Locate and identify every blood parasite.
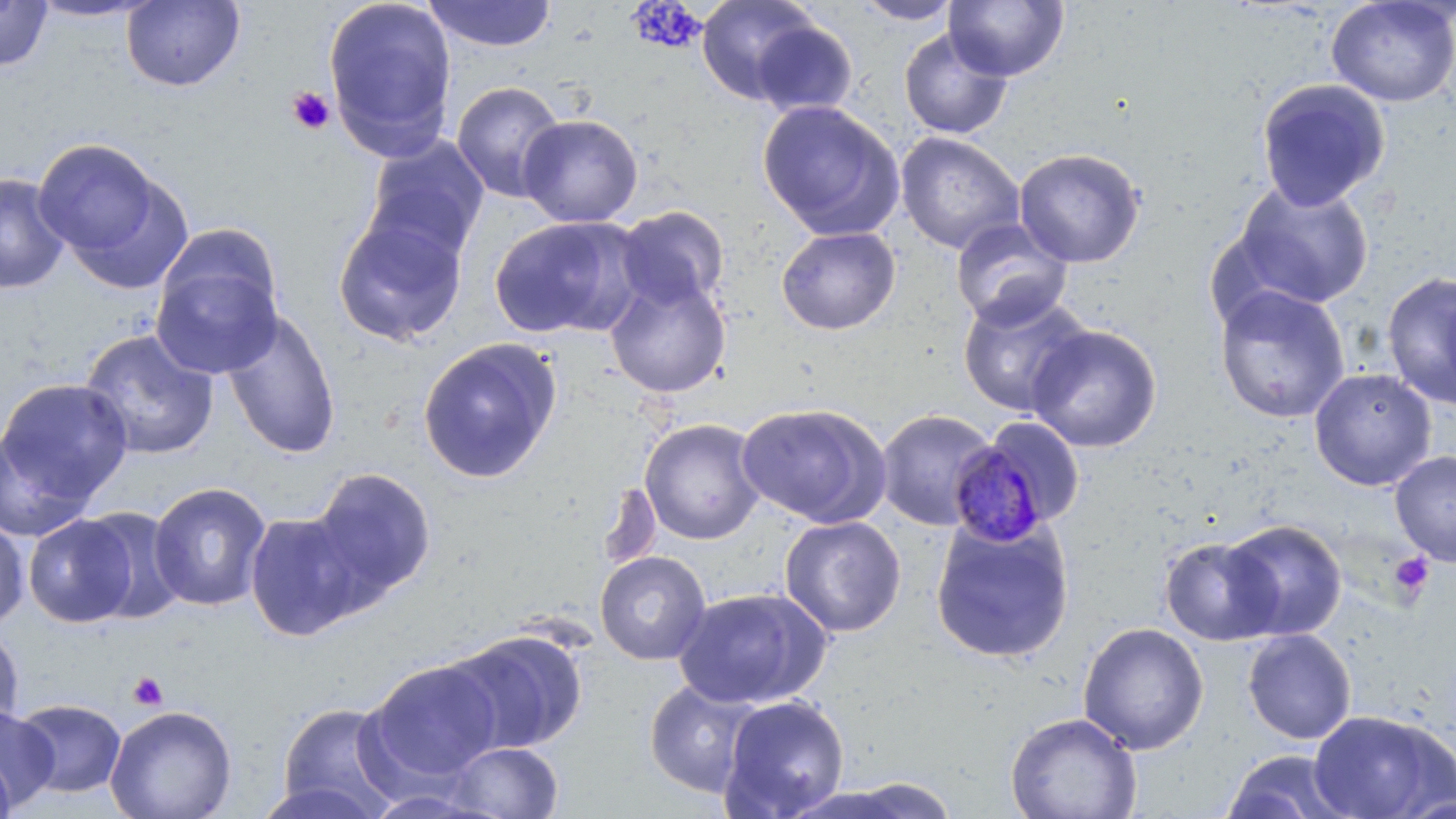

Approximate bounding boxes as [x1, y1, x2, y2] in pixels.
Plasmodium malariae-infected red blood cells: [946, 443, 1052, 549].
No Plasmodium falciparum, Plasmodium ovale, Plasmodium vivax, Babesia divergens, or Trypanosoma brucei observed.

Uninfected red blood cell locations: [322, 0, 458, 158], [421, 0, 558, 53], [695, 0, 821, 104], [851, 0, 964, 25], [1325, 0, 1456, 108], [0, 1, 54, 71], [27, 1, 161, 23], [121, 1, 245, 92], [944, 1, 1069, 82], [748, 18, 859, 119], [898, 27, 1013, 140], [1255, 77, 1391, 211], [450, 80, 567, 203], [757, 99, 905, 241], [518, 114, 644, 227], [895, 131, 1025, 254], [364, 136, 489, 264], [35, 140, 173, 269], [1013, 147, 1145, 268], [0, 173, 70, 295], [1230, 180, 1375, 311], [615, 205, 730, 310], [332, 211, 469, 348], [489, 215, 644, 339], [949, 219, 1074, 330], [775, 226, 902, 336], [149, 245, 284, 379], [1382, 269, 1456, 412], [604, 275, 732, 398], [1214, 285, 1351, 423], [958, 290, 1092, 417], [221, 308, 342, 459], [1025, 324, 1162, 453], [78, 329, 220, 461], [417, 337, 562, 485], [1308, 367, 1437, 491], [1, 377, 133, 515], [735, 403, 892, 528], [875, 409, 998, 531], [640, 419, 765, 545], [996, 420, 1083, 514], [0, 427, 95, 543], [1390, 450, 1456, 566], [307, 467, 437, 602], [148, 481, 272, 612], [598, 481, 662, 576], [77, 506, 186, 625], [244, 511, 364, 641], [23, 513, 139, 628], [0, 515, 30, 630], [779, 515, 907, 637], [930, 515, 1076, 664], [1222, 518, 1347, 641], [1159, 536, 1282, 646], [594, 550, 712, 665], [672, 587, 831, 709], [1077, 622, 1210, 755], [0, 624, 25, 735], [1242, 628, 1357, 745], [444, 629, 588, 754], [363, 659, 503, 785], [643, 679, 762, 798], [718, 694, 851, 818], [11, 698, 127, 798], [275, 701, 403, 817], [105, 704, 237, 819], [0, 707, 59, 812], [1307, 709, 1454, 819], [1005, 711, 1142, 819], [445, 741, 564, 819], [1219, 749, 1358, 819], [0, 757, 16, 819], [813, 776, 964, 818], [250, 779, 388, 819]. Platelet locations: [286, 86, 335, 134], [1389, 552, 1435, 602], [127, 671, 169, 712]. Slide-level diagnosis: Plasmodium malariae. Optical microscopy. Captured at 1000x magnification. Thin blood film. One field of a larger specimen. May-Grünwald-Giemsa stain. Image is 1456×819 pixels.